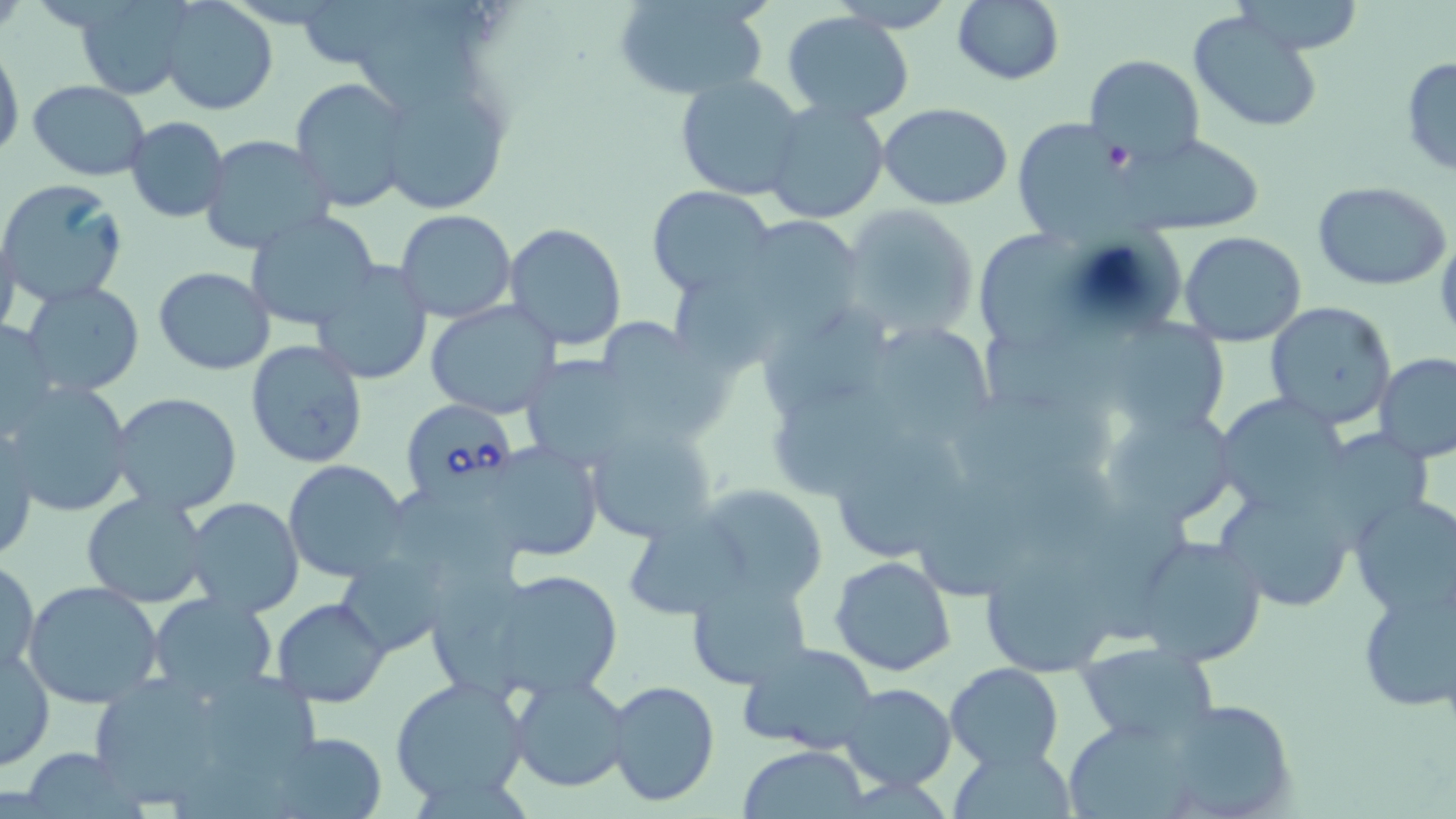

slide-level diagnosis = Babesia divergens
preparation = thin blood film
Babesia divergens-infected red blood cell locations = approximate bounding boxes as named x1/y1/x2/y2 corners in pixels: (x1=400, y1=400, x2=517, y2=502)
magnification = 1000x
image size = 1456×819 pixels
field of view = single
uninfected red blood cell locations = approximate bounding boxes as named x1/y1/x2/y2 corners in pixels: (x1=72, y1=0, x2=196, y2=100), (x1=952, y1=0, x2=1065, y2=87), (x1=158, y1=1, x2=278, y2=115), (x1=359, y1=1, x2=502, y2=115), (x1=613, y1=2, x2=770, y2=102), (x1=1188, y1=9, x2=1326, y2=132), (x1=783, y1=12, x2=916, y2=125), (x1=0, y1=47, x2=22, y2=159), (x1=1084, y1=55, x2=1205, y2=167), (x1=1400, y1=55, x2=1456, y2=178), (x1=675, y1=73, x2=807, y2=202), (x1=290, y1=77, x2=412, y2=213), (x1=29, y1=80, x2=152, y2=180), (x1=394, y1=100, x2=507, y2=214), (x1=764, y1=101, x2=888, y2=223), (x1=879, y1=103, x2=1014, y2=210), (x1=1010, y1=116, x2=1132, y2=235), (x1=125, y1=117, x2=230, y2=222), (x1=1123, y1=132, x2=1265, y2=235), (x1=199, y1=134, x2=334, y2=255), (x1=0, y1=178, x2=128, y2=307), (x1=1316, y1=179, x2=1450, y2=279), (x1=647, y1=185, x2=773, y2=296), (x1=838, y1=203, x2=983, y2=344), (x1=243, y1=210, x2=380, y2=334), (x1=394, y1=210, x2=516, y2=321), (x1=735, y1=216, x2=863, y2=334), (x1=0, y1=224, x2=21, y2=342), (x1=503, y1=224, x2=629, y2=350), (x1=979, y1=226, x2=1094, y2=348), (x1=1178, y1=232, x2=1307, y2=347), (x1=312, y1=261, x2=435, y2=385), (x1=153, y1=267, x2=274, y2=375), (x1=676, y1=270, x2=782, y2=379), (x1=20, y1=282, x2=146, y2=398), (x1=426, y1=302, x2=561, y2=420), (x1=1265, y1=302, x2=1400, y2=430), (x1=760, y1=305, x2=891, y2=416), (x1=1, y1=317, x2=58, y2=438), (x1=1113, y1=318, x2=1229, y2=437), (x1=983, y1=320, x2=1140, y2=419), (x1=603, y1=322, x2=730, y2=440), (x1=879, y1=327, x2=991, y2=441), (x1=245, y1=340, x2=369, y2=469), (x1=1374, y1=353, x2=1456, y2=461), (x1=531, y1=355, x2=657, y2=466), (x1=6, y1=381, x2=134, y2=517), (x1=772, y1=382, x2=908, y2=496), (x1=955, y1=388, x2=1126, y2=477), (x1=109, y1=393, x2=243, y2=515), (x1=1213, y1=393, x2=1351, y2=516), (x1=1101, y1=401, x2=1242, y2=531), (x1=583, y1=423, x2=718, y2=544), (x1=0, y1=424, x2=38, y2=563), (x1=1312, y1=427, x2=1438, y2=542), (x1=837, y1=428, x2=971, y2=554), (x1=480, y1=439, x2=605, y2=562), (x1=283, y1=459, x2=409, y2=581), (x1=959, y1=465, x2=1136, y2=561), (x1=393, y1=484, x2=527, y2=587), (x1=693, y1=484, x2=831, y2=603), (x1=1215, y1=486, x2=1357, y2=613), (x1=82, y1=492, x2=213, y2=609), (x1=1348, y1=494, x2=1456, y2=618), (x1=185, y1=497, x2=305, y2=620), (x1=617, y1=508, x2=755, y2=622), (x1=1130, y1=534, x2=1269, y2=667), (x1=973, y1=546, x2=1128, y2=682), (x1=432, y1=556, x2=553, y2=698), (x1=830, y1=556, x2=958, y2=677), (x1=1, y1=558, x2=39, y2=678), (x1=342, y1=559, x2=451, y2=654), (x1=473, y1=566, x2=625, y2=700), (x1=686, y1=572, x2=813, y2=689), (x1=1354, y1=579, x2=1455, y2=711), (x1=24, y1=580, x2=164, y2=708), (x1=148, y1=594, x2=278, y2=703), (x1=273, y1=598, x2=388, y2=706), (x1=738, y1=641, x2=882, y2=755), (x1=1076, y1=641, x2=1220, y2=744), (x1=0, y1=647, x2=54, y2=770), (x1=944, y1=662, x2=1064, y2=772), (x1=82, y1=664, x2=315, y2=815), (x1=509, y1=674, x2=630, y2=792), (x1=389, y1=675, x2=530, y2=807), (x1=608, y1=679, x2=720, y2=806), (x1=839, y1=684, x2=957, y2=792), (x1=1159, y1=700, x2=1296, y2=818), (x1=1061, y1=716, x2=1211, y2=819), (x1=267, y1=730, x2=391, y2=818), (x1=946, y1=744, x2=1075, y2=817), (x1=738, y1=745, x2=870, y2=819), (x1=21, y1=748, x2=147, y2=817)
modality = light microscopy
stain = May-Grünwald-Giemsa